Outline each blood parasite and name the species.
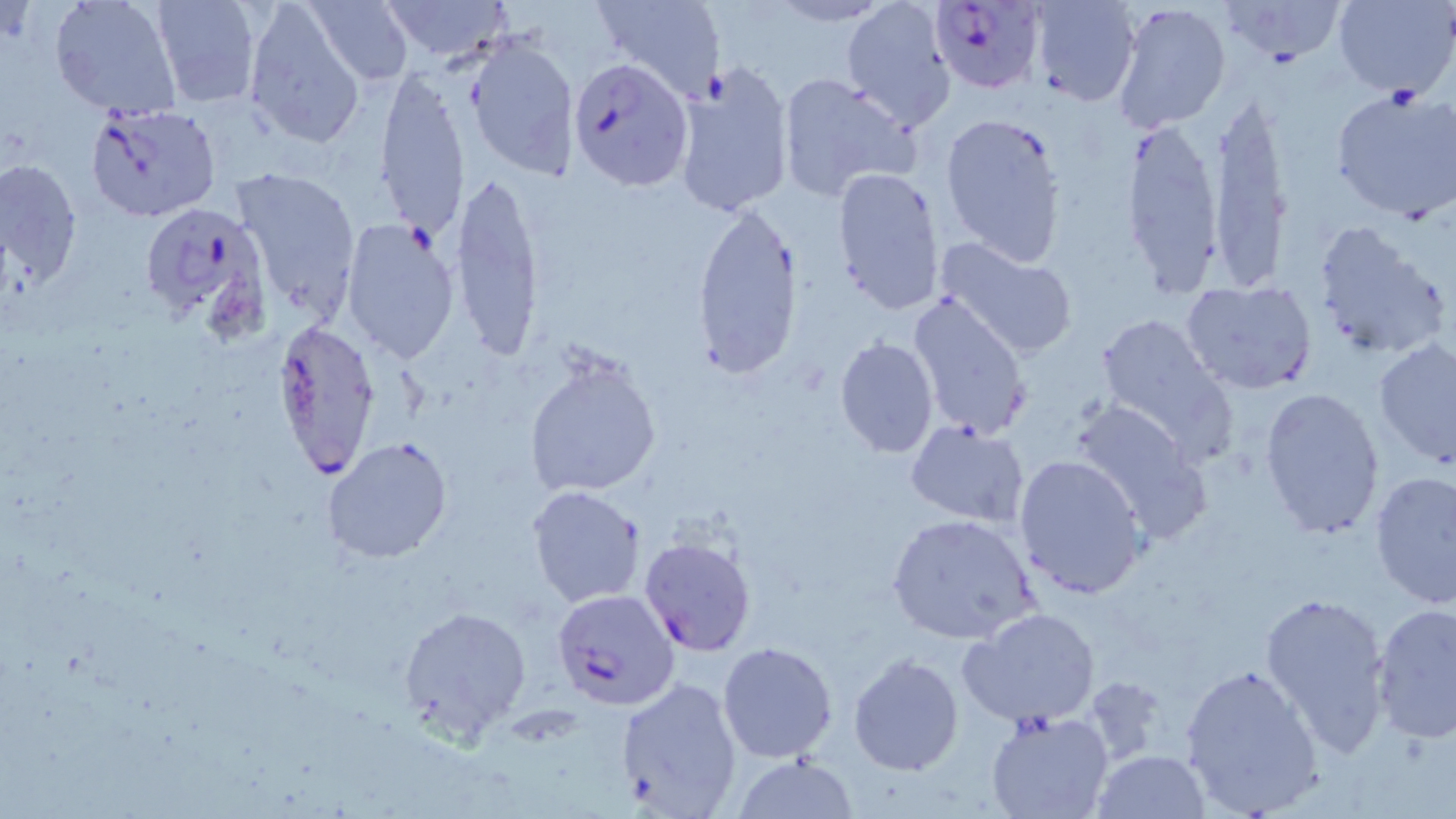

Approximate bounding boxes as named x1/y1/x2/y2 corners in pixels.
Plasmodium falciparum-infected red blood cells: (x1=926, y1=1, x2=1044, y2=98), (x1=570, y1=58, x2=693, y2=191), (x1=84, y1=101, x2=222, y2=224), (x1=137, y1=203, x2=270, y2=329), (x1=271, y1=322, x2=383, y2=484), (x1=553, y1=589, x2=680, y2=710).
No Plasmodium ovale, Plasmodium malariae, Plasmodium vivax, Babesia divergens, or Trypanosoma brucei observed.

Summary:
  - Uninfected red blood cell locations: (x1=48, y1=0, x2=183, y2=120), (x1=150, y1=0, x2=262, y2=107), (x1=302, y1=0, x2=416, y2=87), (x1=380, y1=0, x2=514, y2=63), (x1=593, y1=0, x2=726, y2=101), (x1=840, y1=0, x2=960, y2=131), (x1=1027, y1=0, x2=1140, y2=106), (x1=1111, y1=0, x2=1232, y2=133), (x1=1219, y1=0, x2=1345, y2=65), (x1=1332, y1=0, x2=1454, y2=100), (x1=242, y1=1, x2=365, y2=148), (x1=463, y1=33, x2=581, y2=179), (x1=672, y1=60, x2=795, y2=216), (x1=372, y1=69, x2=468, y2=238), (x1=775, y1=72, x2=920, y2=200), (x1=1330, y1=89, x2=1456, y2=223), (x1=1206, y1=97, x2=1294, y2=289), (x1=940, y1=112, x2=1067, y2=267), (x1=1120, y1=119, x2=1226, y2=294), (x1=1, y1=160, x2=82, y2=290), (x1=232, y1=165, x2=361, y2=320), (x1=831, y1=166, x2=946, y2=313), (x1=450, y1=173, x2=545, y2=363), (x1=692, y1=201, x2=803, y2=379), (x1=341, y1=218, x2=460, y2=366), (x1=1313, y1=221, x2=1450, y2=363), (x1=935, y1=236, x2=1081, y2=360), (x1=1178, y1=280, x2=1318, y2=397), (x1=907, y1=290, x2=1033, y2=443), (x1=1093, y1=314, x2=1231, y2=449), (x1=834, y1=336, x2=940, y2=458), (x1=1373, y1=340, x2=1456, y2=465), (x1=523, y1=350, x2=662, y2=500), (x1=1258, y1=385, x2=1385, y2=538), (x1=1070, y1=400, x2=1211, y2=543), (x1=907, y1=419, x2=1030, y2=526), (x1=321, y1=437, x2=453, y2=563), (x1=1013, y1=453, x2=1149, y2=600), (x1=1369, y1=471, x2=1456, y2=609), (x1=527, y1=484, x2=646, y2=608), (x1=888, y1=513, x2=1038, y2=646), (x1=639, y1=534, x2=759, y2=658), (x1=1259, y1=589, x2=1393, y2=756), (x1=1371, y1=603, x2=1456, y2=742), (x1=396, y1=604, x2=531, y2=739), (x1=960, y1=607, x2=1101, y2=729), (x1=717, y1=641, x2=838, y2=763), (x1=849, y1=652, x2=964, y2=775), (x1=1180, y1=661, x2=1324, y2=816), (x1=613, y1=675, x2=743, y2=816), (x1=1081, y1=678, x2=1169, y2=766), (x1=983, y1=710, x2=1113, y2=819), (x1=1092, y1=749, x2=1211, y2=818), (x1=733, y1=754, x2=858, y2=818)
  - Slide-level diagnosis: Plasmodium falciparum
  - Preparation: thin blood film
  - Magnification: 1000x
  - Stain: May-Grünwald-Giemsa
  - Image size: 1456×819 pixels
  - Field of view: single
  - Modality: optical microscopy